Mark where platelets are.
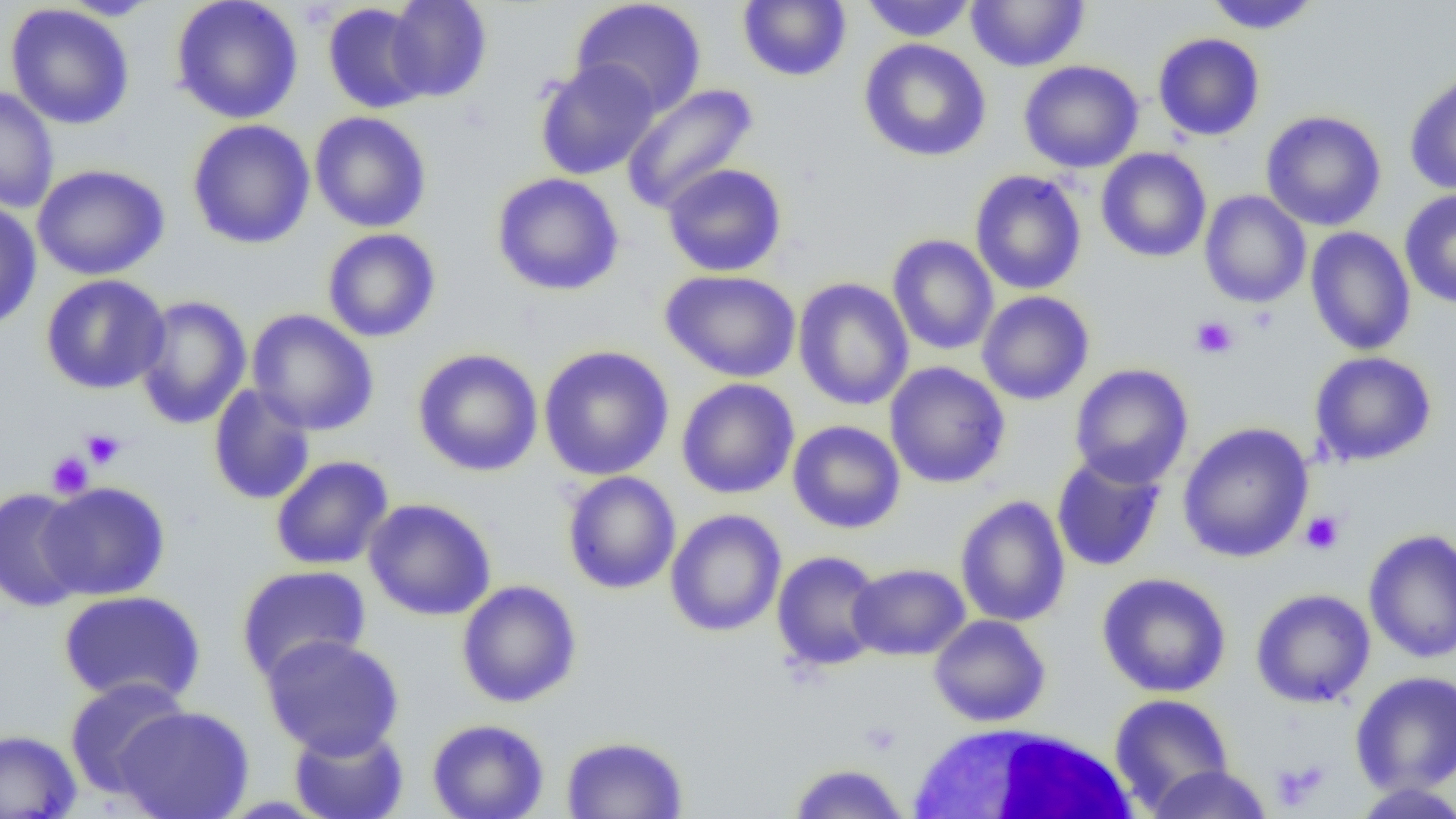
Approximate bounding boxes as named x1/y1/x2/y2 corners in pixels.
Platelets: (x1=1190, y1=315, x2=1239, y2=359), (x1=81, y1=428, x2=126, y2=469), (x1=46, y1=451, x2=93, y2=498), (x1=1300, y1=510, x2=1345, y2=555), (x1=1269, y1=759, x2=1329, y2=811).

Uninfected red blood cell locations: (x1=170, y1=0, x2=304, y2=124), (x1=384, y1=0, x2=493, y2=103), (x1=570, y1=0, x2=708, y2=117), (x1=859, y1=0, x2=977, y2=42), (x1=965, y1=0, x2=1090, y2=73), (x1=1202, y1=0, x2=1322, y2=34), (x1=58, y1=1, x2=165, y2=20), (x1=738, y1=1, x2=851, y2=82), (x1=322, y1=3, x2=432, y2=114), (x1=5, y1=4, x2=135, y2=130), (x1=1152, y1=33, x2=1265, y2=141), (x1=859, y1=38, x2=992, y2=162), (x1=534, y1=59, x2=661, y2=181), (x1=1018, y1=60, x2=1144, y2=173), (x1=1404, y1=71, x2=1456, y2=196), (x1=620, y1=82, x2=759, y2=215), (x1=0, y1=86, x2=59, y2=214), (x1=1260, y1=110, x2=1387, y2=231), (x1=309, y1=111, x2=432, y2=233), (x1=186, y1=119, x2=316, y2=250), (x1=1096, y1=147, x2=1212, y2=263), (x1=32, y1=163, x2=170, y2=281), (x1=661, y1=163, x2=787, y2=277), (x1=969, y1=169, x2=1087, y2=295), (x1=491, y1=172, x2=625, y2=296), (x1=1399, y1=189, x2=1456, y2=308), (x1=1199, y1=190, x2=1311, y2=308), (x1=0, y1=199, x2=42, y2=332), (x1=1304, y1=226, x2=1416, y2=356), (x1=322, y1=228, x2=441, y2=342), (x1=887, y1=234, x2=999, y2=355), (x1=660, y1=270, x2=801, y2=382), (x1=40, y1=274, x2=170, y2=395), (x1=793, y1=277, x2=914, y2=411), (x1=977, y1=290, x2=1094, y2=405), (x1=134, y1=294, x2=252, y2=430), (x1=247, y1=309, x2=379, y2=435), (x1=538, y1=344, x2=675, y2=481), (x1=412, y1=348, x2=543, y2=477), (x1=1308, y1=351, x2=1437, y2=466), (x1=884, y1=361, x2=1011, y2=489), (x1=1069, y1=363, x2=1193, y2=488), (x1=676, y1=378, x2=800, y2=499), (x1=207, y1=384, x2=316, y2=506), (x1=787, y1=420, x2=906, y2=534), (x1=1177, y1=422, x2=1314, y2=563), (x1=1051, y1=453, x2=1166, y2=571), (x1=270, y1=455, x2=394, y2=570), (x1=562, y1=470, x2=681, y2=595), (x1=37, y1=481, x2=170, y2=600), (x1=0, y1=487, x2=92, y2=613), (x1=954, y1=494, x2=1070, y2=627), (x1=363, y1=498, x2=497, y2=621), (x1=665, y1=508, x2=787, y2=637), (x1=1363, y1=528, x2=1456, y2=664), (x1=771, y1=550, x2=886, y2=672), (x1=848, y1=563, x2=970, y2=661), (x1=235, y1=564, x2=372, y2=685), (x1=1096, y1=572, x2=1232, y2=698), (x1=456, y1=579, x2=582, y2=708), (x1=1250, y1=588, x2=1376, y2=708), (x1=57, y1=590, x2=207, y2=707), (x1=929, y1=615, x2=1051, y2=727), (x1=260, y1=634, x2=404, y2=759), (x1=1349, y1=670, x2=1456, y2=796), (x1=64, y1=677, x2=193, y2=799), (x1=1109, y1=693, x2=1235, y2=813), (x1=113, y1=705, x2=255, y2=819), (x1=426, y1=718, x2=549, y2=819), (x1=289, y1=724, x2=409, y2=819), (x1=0, y1=728, x2=82, y2=818), (x1=560, y1=735, x2=689, y2=818), (x1=786, y1=762, x2=910, y2=818), (x1=1145, y1=763, x2=1273, y2=819), (x1=1350, y1=782, x2=1456, y2=818). White blood cell locations: (x1=906, y1=721, x2=1141, y2=817). Slide-level diagnosis: no evidence of blood parasites. Single field of view. Thin blood smear. Light microscopy. 1000x magnification. Image is 1456×819 pixels.